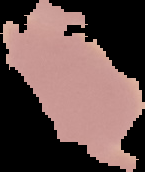 From a thin blood smear. Image is 145×172 pixels. Result: negative for Plasmodium parasites. The area outside the segmented cell region is set to black.